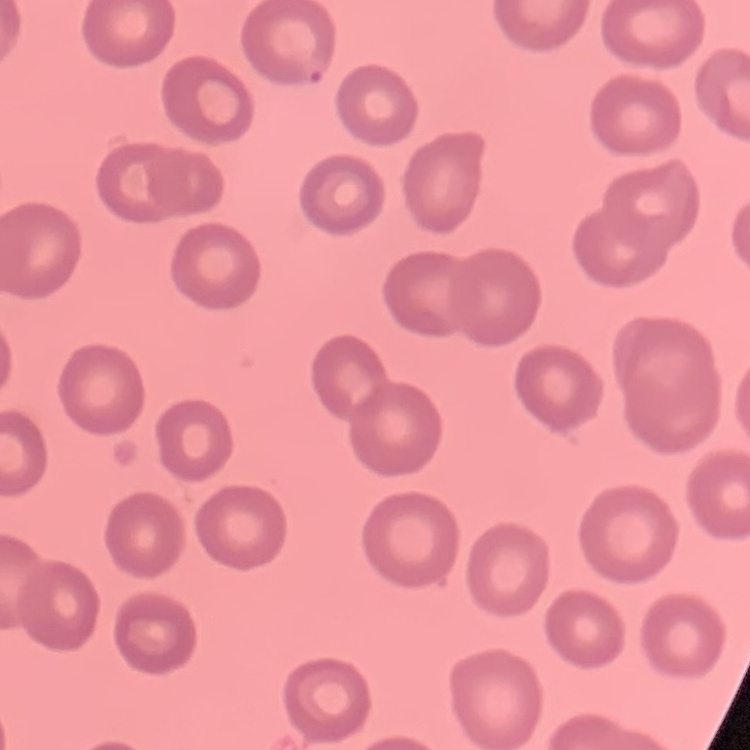
red blood cell morphology = no rouleaux formation
image type = square crop of a larger photomicrograph
preparation = thin blood film
stain = Field's or Giemsa